State which parasite is depicted.
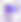

This is Toxoplasma gondii.

Captured at 400x magnification. Photomicrograph.